Locate every blood parasite and identify its species.
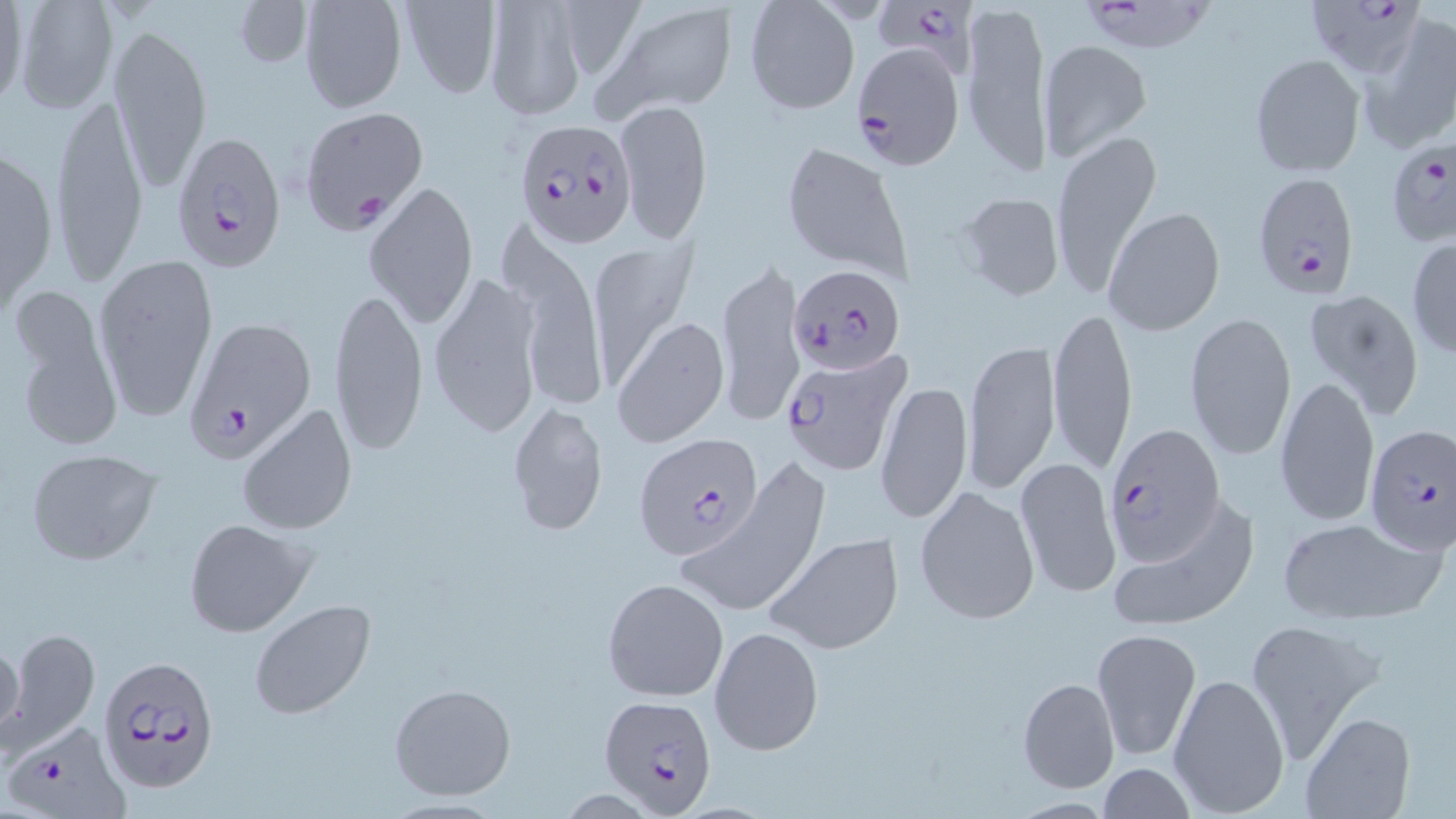

Approximate bounding boxes as (x1, y1, x2, y2) in pixels.
Plasmodium falciparum-infected red blood cells: (871, 0, 979, 78), (1082, 0, 1220, 58), (1307, 1, 1424, 80), (847, 43, 966, 171), (299, 106, 429, 232), (515, 118, 636, 249), (169, 130, 286, 268), (1384, 137, 1456, 249), (1252, 172, 1361, 298), (785, 264, 908, 376), (182, 316, 317, 462), (777, 346, 911, 476), (1105, 422, 1224, 562), (1362, 424, 1454, 554), (637, 434, 765, 560), (97, 654, 219, 794), (597, 694, 718, 814), (7, 725, 126, 816).
No Plasmodium ovale, Plasmodium malariae, Plasmodium vivax, Babesia divergens, or Trypanosoma brucei observed.

Summary:
  - Uninfected red blood cell locations: (0, 0, 28, 113), (10, 0, 120, 114), (231, 0, 313, 71), (297, 0, 407, 113), (397, 0, 503, 98), (743, 0, 861, 116), (960, 0, 1053, 183), (483, 1, 589, 119), (601, 4, 736, 117), (1362, 15, 1456, 153), (106, 21, 210, 198), (1038, 39, 1152, 162), (1250, 54, 1364, 177), (51, 95, 149, 284), (615, 99, 713, 244), (1049, 128, 1162, 299), (781, 140, 911, 280), (0, 142, 59, 320), (364, 179, 479, 332), (955, 190, 1066, 303), (1103, 206, 1225, 337), (495, 217, 608, 417), (1406, 236, 1456, 359), (586, 243, 695, 386), (92, 252, 220, 422), (715, 261, 806, 431), (426, 269, 547, 440), (329, 285, 430, 456), (1303, 287, 1425, 419), (8, 291, 122, 452), (1049, 303, 1136, 473), (1184, 310, 1297, 461), (612, 315, 730, 447), (962, 338, 1060, 498), (1275, 373, 1380, 526), (876, 377, 973, 525), (507, 400, 609, 538), (237, 401, 357, 536), (26, 450, 164, 565), (1014, 455, 1122, 599), (675, 463, 834, 619), (914, 483, 1041, 627), (1105, 495, 1261, 634), (1277, 516, 1445, 625), (182, 517, 316, 639), (764, 531, 906, 655), (602, 576, 729, 702), (249, 600, 376, 721), (1243, 616, 1389, 762), (709, 625, 825, 758), (6, 627, 99, 752), (1091, 628, 1202, 763), (0, 635, 25, 751), (1169, 672, 1289, 813), (1017, 676, 1119, 792), (389, 680, 517, 801), (1300, 710, 1414, 819), (1096, 762, 1194, 819)
  - Slide-level diagnosis: Plasmodium falciparum
  - Preparation: thin blood smear
  - Magnification: 1000x
  - Image size: 1456×819 pixels
  - Field of view: single
  - Stain: May-Grünwald-Giemsa
  - Modality: optical microscopy